Report the malaria status of this cell.
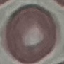

Uninfected.

Summary:
  - Capture: smartphone through the microscope eyepiece
  - Stain: Giemsa
  - Preparation: thin blood film
  - Image type: cell patch, automatically extracted from a larger field of view and resized to 64 × 64 pixels